Classify this cell by malaria status.
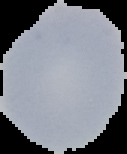

It is uninfected.

{
  "image_size": "127×154 pixels",
  "image_type": "segmented cell region on a black background",
  "preparation": "thin blood film"
}